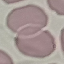

Summary:
  - Malaria status: uninfected
  - Stain: Giemsa
  - Capture: smartphone camera at the microscope eyepiece
  - Preparation: thin blood smear
  - Image type: automatically extracted cell patch, resized to 64 × 64 pixels